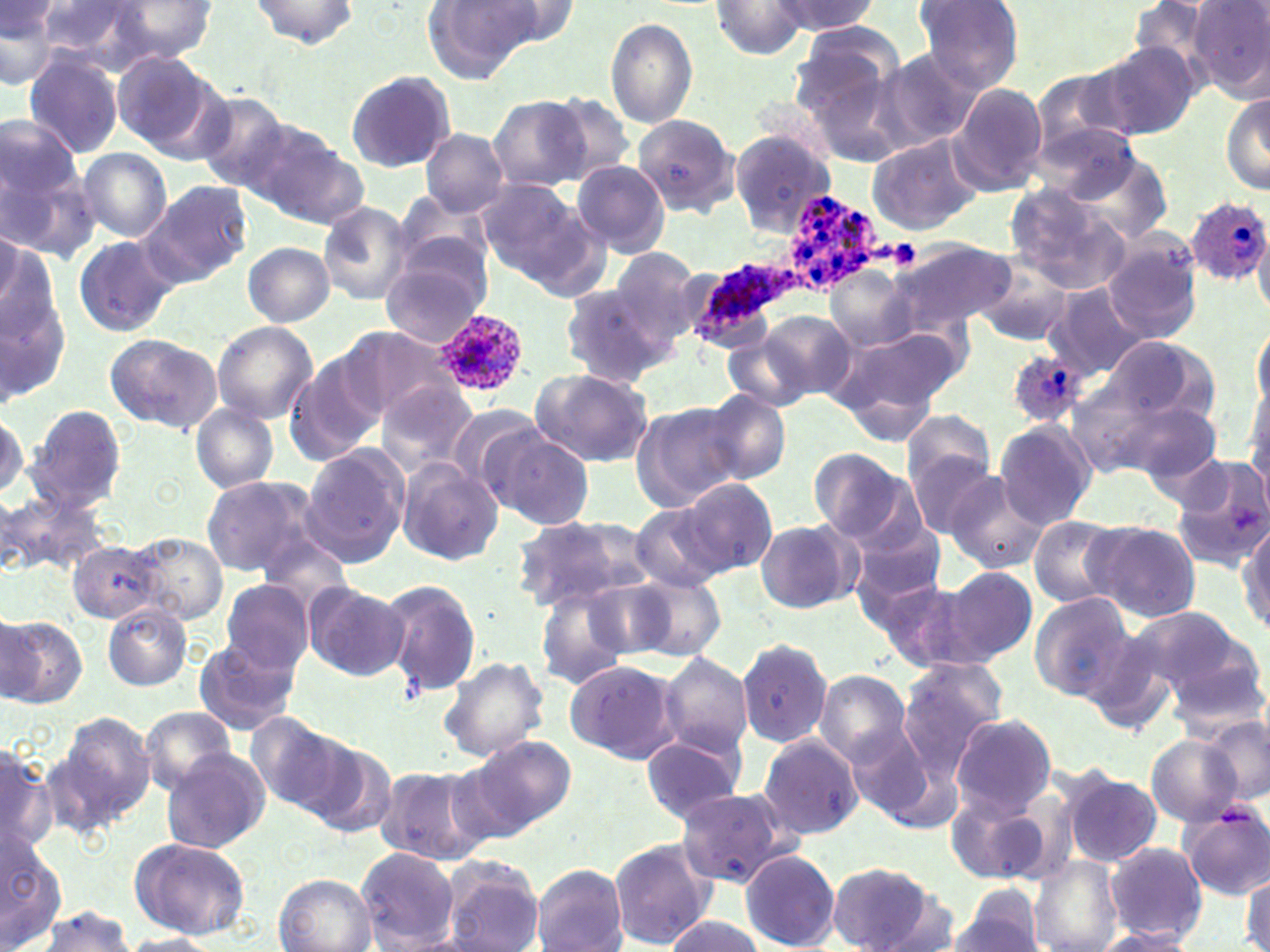
Summary:
  - Coordinate format: approximate bounding boxes as (x1, y1, x2, y2) in pixels
  - Uninfected red blood cell locations: (250, 0, 358, 48), (423, 0, 544, 80), (912, 0, 1023, 94), (33, 1, 149, 72), (113, 1, 218, 60), (469, 1, 581, 50), (710, 1, 811, 59), (772, 1, 879, 35), (1, 2, 60, 87), (1191, 2, 1270, 100), (605, 18, 697, 129), (790, 27, 900, 118), (1092, 44, 1200, 143), (113, 51, 216, 151), (882, 51, 986, 148), (22, 52, 124, 160), (1033, 69, 1130, 158), (344, 70, 456, 174), (949, 84, 1048, 195), (1220, 87, 1270, 197), (192, 92, 294, 193), (543, 92, 634, 181), (487, 96, 589, 192), (0, 114, 81, 206), (632, 116, 738, 220), (1031, 122, 1149, 210), (243, 123, 363, 225), (421, 128, 509, 216), (730, 132, 834, 234), (866, 134, 982, 235), (77, 149, 172, 242), (0, 152, 97, 263), (1062, 152, 1172, 246), (573, 160, 670, 257), (477, 179, 592, 285), (142, 181, 253, 289), (1006, 185, 1124, 295), (393, 195, 492, 286), (318, 203, 412, 307), (1254, 226, 1270, 317), (1100, 233, 1203, 343), (73, 237, 177, 336), (887, 238, 1014, 339), (0, 240, 71, 404), (243, 241, 336, 327), (611, 249, 707, 343), (381, 250, 492, 346), (977, 261, 1076, 345), (825, 265, 915, 347), (1041, 284, 1149, 379), (559, 285, 672, 388), (732, 309, 842, 453), (758, 312, 855, 402), (212, 321, 318, 424), (827, 321, 965, 438), (1253, 324, 1270, 414), (340, 326, 457, 423), (104, 333, 222, 433), (1098, 336, 1216, 431), (730, 337, 810, 411), (284, 352, 386, 466), (531, 369, 653, 467), (1245, 374, 1270, 502), (375, 380, 478, 478), (700, 390, 791, 485), (1121, 397, 1225, 491), (190, 403, 280, 493), (630, 403, 744, 511), (26, 404, 127, 516), (445, 405, 547, 499), (900, 409, 999, 525), (993, 421, 1098, 528), (487, 431, 596, 532), (299, 444, 411, 570), (807, 447, 913, 543), (1168, 457, 1270, 569), (393, 458, 503, 566), (942, 472, 1050, 574), (200, 475, 322, 579), (680, 478, 777, 577), (0, 490, 92, 579), (627, 502, 730, 593), (1027, 514, 1126, 607), (510, 516, 644, 612), (755, 519, 861, 614), (1236, 519, 1269, 637), (1087, 520, 1202, 622), (847, 527, 946, 616), (132, 534, 228, 626), (66, 537, 166, 626), (941, 566, 1038, 664), (628, 572, 726, 661), (873, 578, 985, 674), (218, 579, 316, 675), (302, 580, 410, 681), (380, 580, 481, 696), (534, 585, 632, 691), (1028, 592, 1136, 702), (103, 604, 192, 691), (1148, 609, 1266, 722), (1, 615, 88, 707), (737, 636, 832, 749), (192, 637, 300, 735), (657, 652, 753, 759), (439, 655, 550, 763), (565, 659, 683, 764), (894, 659, 1007, 780), (812, 669, 914, 768), (140, 706, 239, 795), (48, 711, 155, 832), (245, 713, 356, 814), (951, 714, 1056, 815), (1201, 715, 1269, 805), (847, 723, 940, 825), (274, 728, 390, 831), (757, 733, 865, 839), (469, 735, 575, 834), (641, 735, 743, 823), (1147, 736, 1243, 826), (0, 745, 56, 855), (161, 748, 270, 854), (442, 754, 547, 848), (375, 765, 492, 867), (1061, 770, 1162, 867), (675, 787, 792, 888), (945, 787, 1048, 884), (1179, 799, 1270, 900), (0, 837, 67, 952), (608, 838, 716, 950), (124, 839, 250, 940), (1106, 842, 1208, 942), (355, 847, 458, 950), (740, 848, 840, 951), (1028, 855, 1124, 952), (438, 857, 545, 952), (827, 861, 940, 951), (529, 864, 628, 952), (1241, 869, 1269, 952), (272, 873, 376, 952), (952, 886, 1046, 952), (34, 905, 136, 952), (662, 915, 764, 951), (1088, 929, 1198, 952), (119, 934, 220, 952)
  - Plasmodium ovale-infected red blood cell locations: (778, 190, 883, 297), (1184, 195, 1270, 285), (688, 256, 795, 347), (429, 309, 530, 400), (1006, 349, 1086, 427)
  - Slide-level diagnosis: Plasmodium ovale
  - Stain: May-Grünwald-Giemsa
  - Modality: light microscopy
  - Preparation: thin blood smear
  - Magnification: 1000x
  - Image size: 1270×952 pixels
  - Field of view: one of a larger specimen